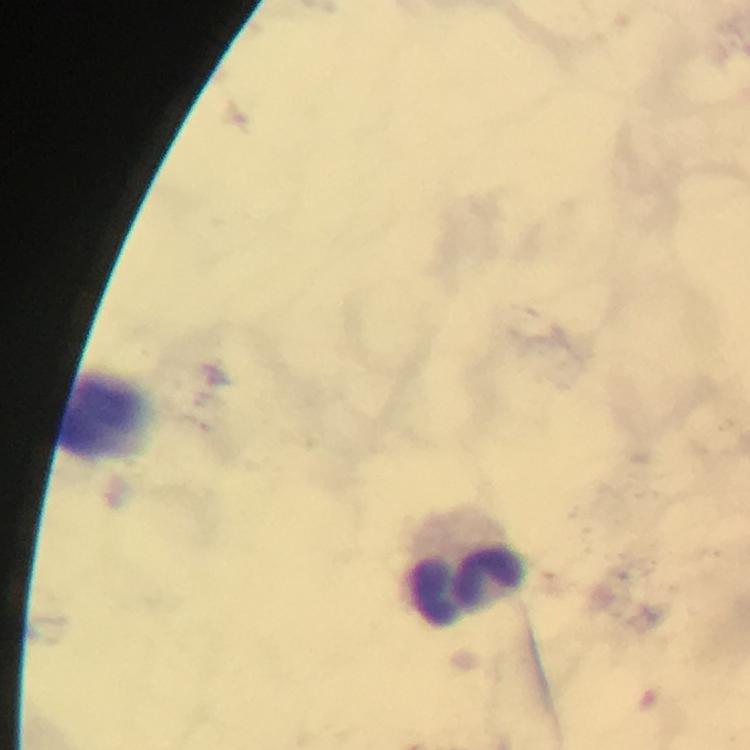
preparation = thick blood smear
magnification = 100x
leukocyte locations = approximate centers as {x, y} in pixels: {97, 422}, {466, 579}
cropped from = one field of view
Plasmodium parasites = none seen
stain = Giemsa
image size = 750×750 pixels
immersion oil = used
capture = smartphone photograph through a microscope
context = from a diagnostic examination for malaria